Name the cell type shown.
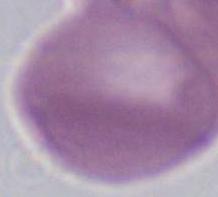
An erythrocyte.

magnification = 1000x
modality = photomicrograph